Assess this cell for malaria.
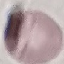

It is uninfected.

Summary:
  - Stain: Giemsa
  - Preparation: thin blood smear
  - Capture: smartphone camera at the microscope eyepiece
  - Image type: cell patch, automatically extracted from a larger field of view and resized to 64 × 64 pixels